Locate every blood parasite and identify its species.
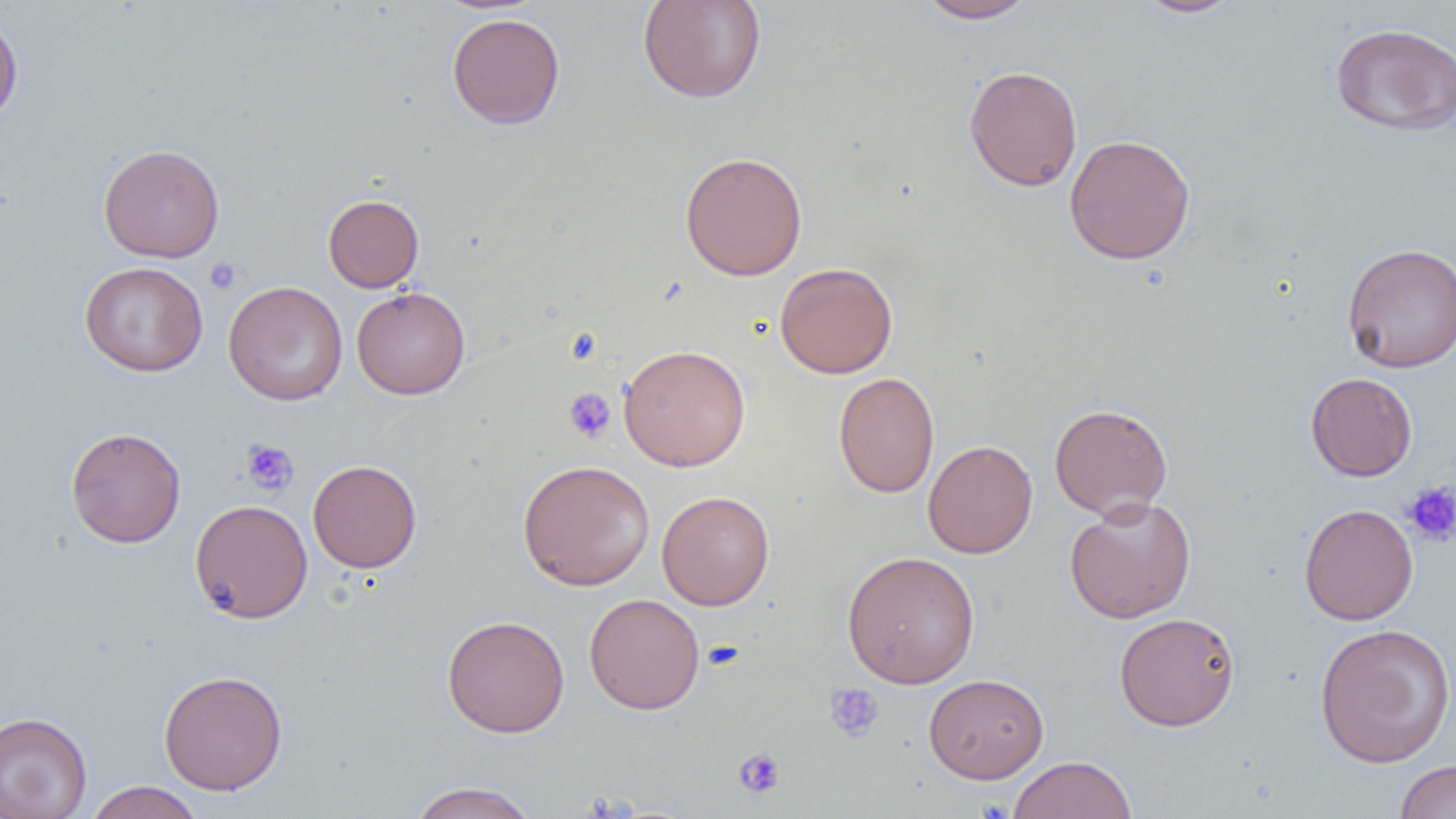
No blood parasites seen.

Summary:
  - Coordinate format: approximate bounding boxes as named x1/y1/x2/y2 corners in pixels
  - Platelet locations: (x1=204, y1=257, x2=241, y2=295), (x1=564, y1=388, x2=616, y2=443), (x1=241, y1=438, x2=299, y2=497), (x1=1403, y1=480, x2=1456, y2=546), (x1=702, y1=640, x2=744, y2=671), (x1=824, y1=682, x2=885, y2=742), (x1=733, y1=747, x2=786, y2=799)
  - Uninfected red blood cell locations: (x1=637, y1=0, x2=767, y2=104), (x1=914, y1=0, x2=1038, y2=23), (x1=1135, y1=0, x2=1243, y2=18), (x1=446, y1=12, x2=565, y2=129), (x1=0, y1=15, x2=23, y2=126), (x1=1330, y1=22, x2=1456, y2=136), (x1=963, y1=65, x2=1083, y2=191), (x1=1064, y1=133, x2=1196, y2=265), (x1=98, y1=143, x2=225, y2=262), (x1=679, y1=151, x2=808, y2=280), (x1=322, y1=194, x2=424, y2=292), (x1=1341, y1=242, x2=1456, y2=373), (x1=80, y1=261, x2=208, y2=376), (x1=775, y1=261, x2=898, y2=378), (x1=223, y1=281, x2=348, y2=406), (x1=351, y1=286, x2=471, y2=400), (x1=618, y1=344, x2=751, y2=471), (x1=833, y1=371, x2=939, y2=498), (x1=1305, y1=372, x2=1417, y2=481), (x1=1049, y1=403, x2=1173, y2=520), (x1=65, y1=426, x2=186, y2=548), (x1=923, y1=440, x2=1038, y2=559), (x1=308, y1=459, x2=422, y2=573), (x1=517, y1=460, x2=655, y2=591), (x1=657, y1=490, x2=774, y2=611), (x1=1064, y1=495, x2=1197, y2=624), (x1=190, y1=499, x2=312, y2=623), (x1=1299, y1=503, x2=1418, y2=626), (x1=842, y1=550, x2=980, y2=689), (x1=584, y1=593, x2=705, y2=715), (x1=1114, y1=612, x2=1241, y2=731), (x1=441, y1=615, x2=570, y2=737), (x1=1313, y1=623, x2=1456, y2=768), (x1=158, y1=669, x2=288, y2=796), (x1=923, y1=673, x2=1049, y2=783), (x1=0, y1=711, x2=92, y2=819), (x1=1007, y1=755, x2=1137, y2=819), (x1=1394, y1=759, x2=1456, y2=818), (x1=85, y1=781, x2=204, y2=819), (x1=408, y1=781, x2=539, y2=819)
  - Slide-level diagnosis: no evidence of blood parasites
  - Modality: optical microscopy
  - Image size: 1456×819 pixels
  - Magnification: 1000x
  - Field of view: single
  - Preparation: thin blood film